Report the malaria status of this cell.
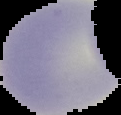

Uninfected.

{
  "image_size": "121×115 pixels",
  "image_type": "cell region segmented out of the field of view; surrounding area masked to black",
  "preparation": "thin blood smear"
}